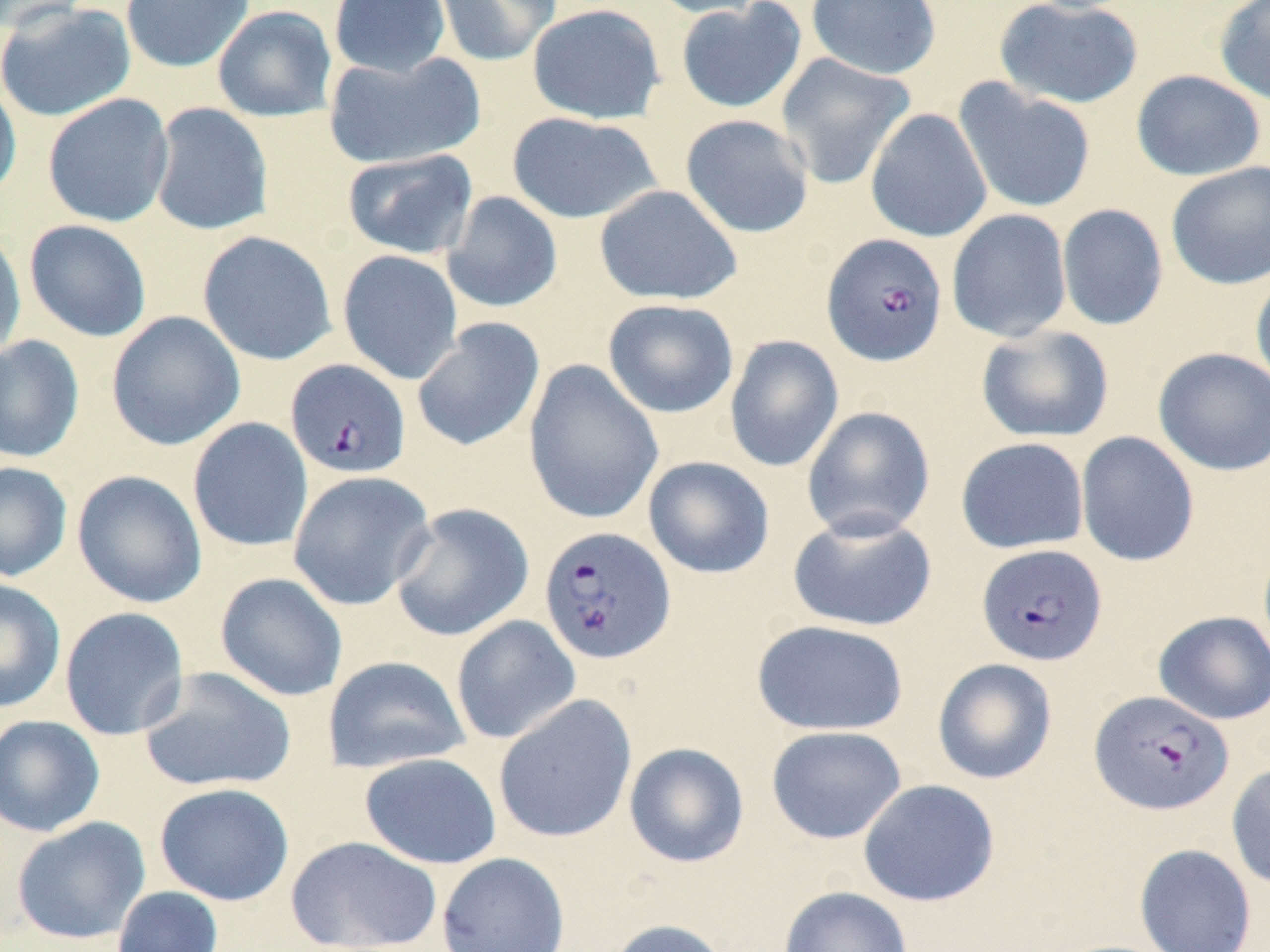

Approximate bounding boxes as [x1, y1, x2, y2] in pixels. Uninfected red blood cell locations: [0, 0, 97, 33], [120, 0, 255, 73], [329, 0, 451, 78], [433, 0, 562, 68], [643, 0, 775, 19], [806, 0, 942, 80], [994, 0, 1144, 109], [1214, 0, 1270, 107], [675, 1, 807, 114], [1, 2, 137, 123], [527, 3, 665, 125], [212, 5, 338, 123], [324, 50, 485, 170], [775, 53, 916, 190], [1131, 70, 1266, 181], [0, 76, 22, 205], [954, 79, 1097, 215], [42, 93, 174, 228], [148, 103, 274, 236], [865, 108, 992, 243], [505, 112, 663, 224], [680, 114, 814, 239], [342, 149, 478, 259], [1166, 162, 1270, 290], [594, 184, 743, 306], [441, 191, 563, 313], [1057, 204, 1168, 331], [947, 209, 1072, 343], [24, 220, 152, 342], [0, 226, 26, 361], [197, 230, 337, 366], [337, 250, 463, 384], [1250, 268, 1270, 396], [602, 299, 739, 418], [106, 311, 246, 451], [411, 317, 545, 453], [975, 325, 1115, 443], [724, 334, 844, 473], [0, 335, 85, 463], [1152, 347, 1270, 476], [522, 359, 664, 525], [801, 406, 936, 541], [187, 417, 313, 553], [1075, 431, 1200, 567], [955, 436, 1089, 554], [643, 456, 775, 579], [0, 461, 73, 582], [72, 470, 207, 609], [287, 470, 436, 611], [389, 503, 534, 642], [787, 510, 938, 632], [215, 572, 348, 702], [0, 578, 66, 714], [59, 606, 189, 740], [1153, 610, 1270, 725], [450, 615, 581, 745], [751, 619, 909, 736], [322, 655, 471, 774], [932, 658, 1058, 785], [138, 666, 296, 793], [492, 694, 637, 844], [0, 714, 105, 837], [765, 725, 906, 844], [624, 742, 749, 868], [359, 752, 502, 869], [1226, 762, 1270, 890], [858, 779, 1000, 907], [154, 783, 294, 906], [12, 817, 151, 944], [285, 835, 443, 952], [1134, 843, 1257, 952], [436, 851, 571, 952], [778, 885, 912, 952], [113, 886, 223, 952], [604, 918, 731, 952]. Plasmodium falciparum-infected red blood cell locations: [821, 233, 948, 366], [285, 358, 411, 479], [538, 526, 676, 665], [976, 543, 1107, 667], [1089, 690, 1234, 816]. Slide-level diagnosis: Plasmodium falciparum. Light microscopy. May-Grünwald-Giemsa-stained preparation. 1000x magnification. One field of a larger specimen. Image is 1270×952 pixels. Thin blood film.